Classify this cell by malaria status.
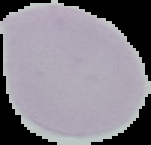

It is uninfected.

Summary:
  - Preparation: thin blood smear
  - Image type: segmented cell region with the area outside set to black
  - Image size: 151×145 pixels